Look for Plasmodium parasites.
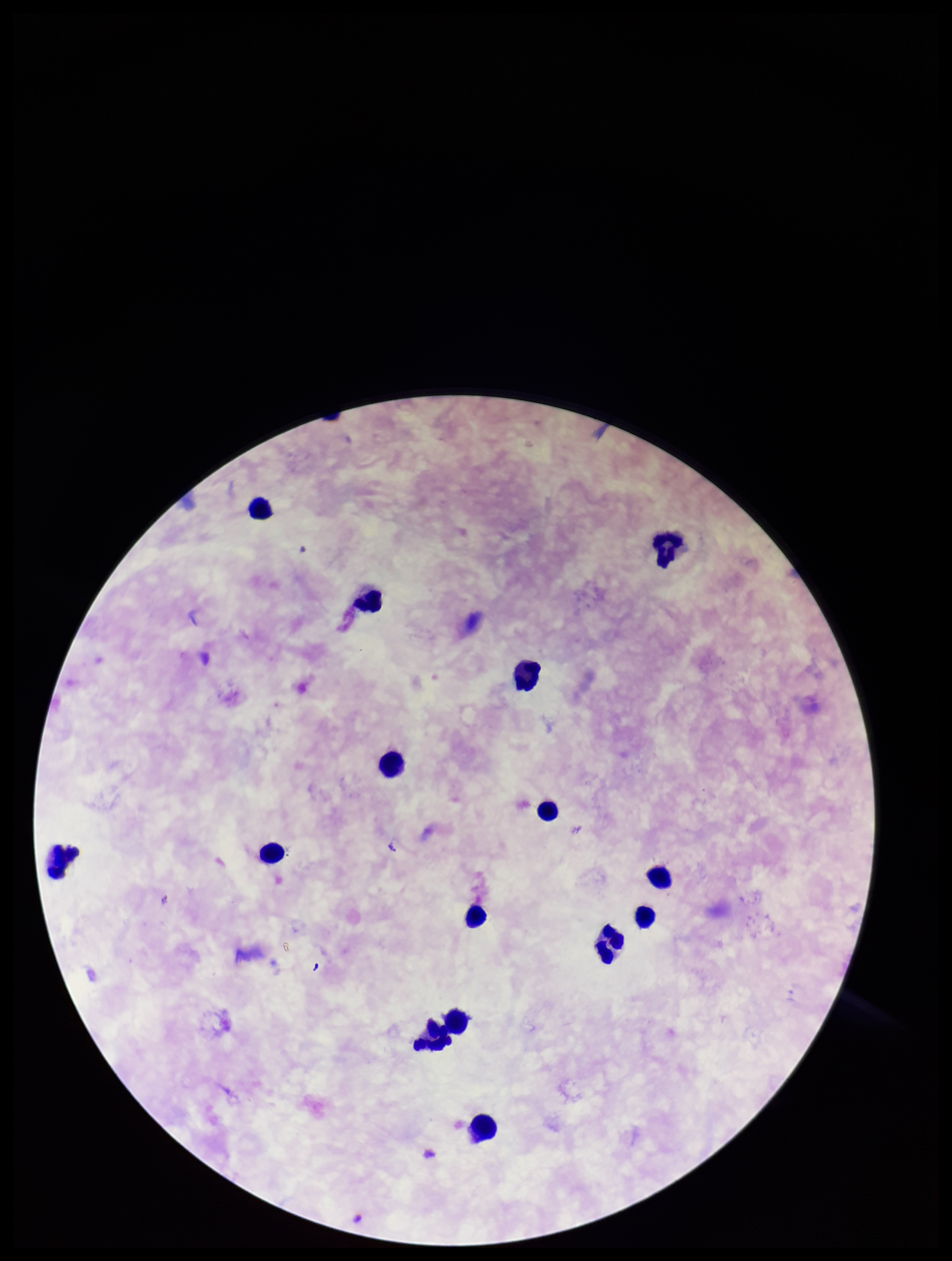

None seen.

parasite count = 0
stain = Giemsa
image size = 952×1261 pixels
leukocyte count = 15
patient malaria status = negative
field of view = single
preparation = thick
capture = smartphone photograph through the microscope eyepiece